Report the malaria status of this cell.
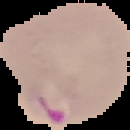
It is parasitized.

Summary:
  - Image type: cell region segmented out of the field of view; surrounding area masked to black
  - Preparation: thin blood film
  - Image size: 130×130 pixels